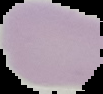
image size = 103×94 pixels
malaria status = uninfected
image type = cell region segmented out of the field of view; surrounding area masked to black
preparation = thin blood smear